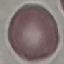

result = no malaria parasites seen
preparation = thin smear
capture = smartphone camera at the microscope eyepiece
image type = automatically extracted cell patch, resized to 64 × 64 pixels
stain = Giemsa